Classify this cell by malaria status.
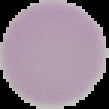
It is uninfected.

preparation = thin blood film
image type = segmented cell region on a black background
image size = 109×109 pixels